State which parasite is depicted.
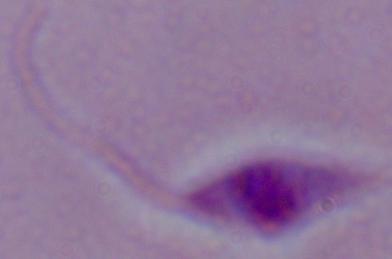

This is Leishmania.

Captured at 1000x magnification. Micrograph.